Give the position of every malaria parasite.
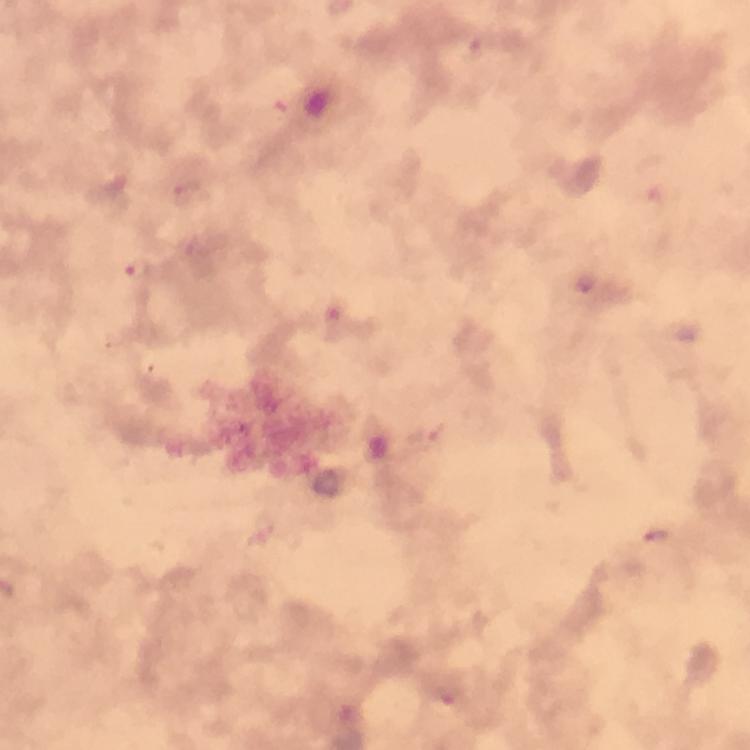

Approximate centers as (x, y) in pixels.
Malaria parasites: (477, 48), (189, 194), (137, 272), (586, 284), (335, 321), (656, 539), (448, 697).

{
  "cropped_from": "a single field of view",
  "context": "from a malaria diagnostic workup",
  "image_size": "750×750 pixels",
  "preparation": "thick blood smear",
  "immersion_oil": "applied",
  "capture": "smartphone camera through the microscope",
  "magnification": "100x",
  "stain": "Giemsa"
}